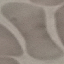

{
  "result": "no malaria parasites detected",
  "image_type": "automatically extracted cell patch, resized to 64 × 64 pixels",
  "stain": "Giemsa",
  "preparation": "thin blood smear",
  "capture": "smartphone camera at the microscope eyepiece"
}